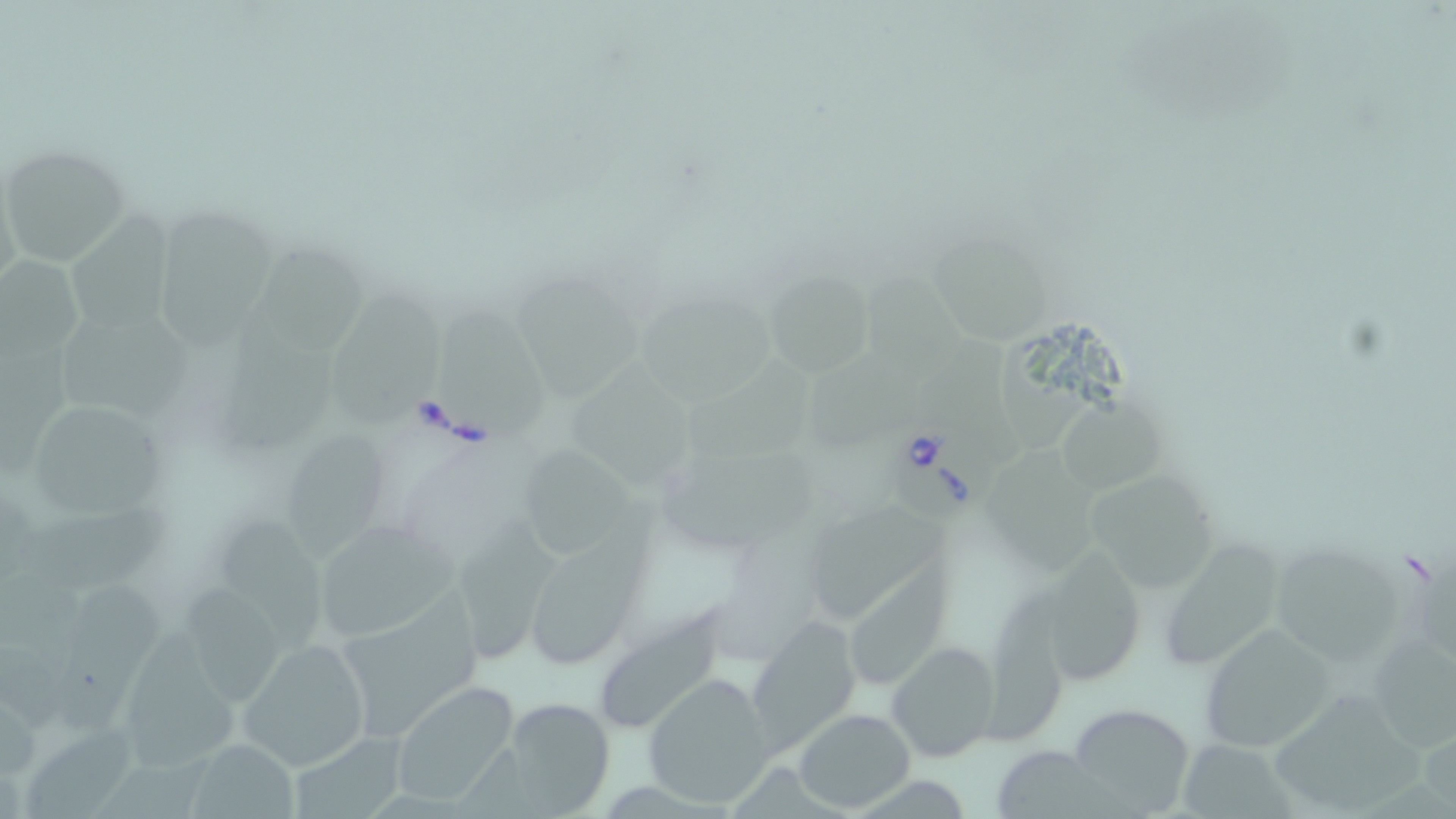

Summary:
  - Coordinate format: approximate bounding boxes as (x1, y1, x2, y2) in pixels
  - Babesia divergens-infected red blood cell locations: (889, 422, 997, 528)
  - Uninfected red blood cell locations: (0, 145, 129, 265), (65, 210, 191, 339), (158, 210, 277, 353), (934, 229, 1051, 347), (262, 245, 365, 353), (1, 254, 84, 360), (513, 271, 644, 409), (764, 272, 876, 375), (332, 276, 444, 427), (866, 279, 967, 378), (640, 288, 776, 409), (438, 299, 553, 435), (59, 308, 202, 425), (219, 311, 344, 454), (918, 334, 1004, 441), (1006, 341, 1095, 446), (0, 344, 76, 481), (692, 353, 820, 474), (569, 358, 696, 487), (813, 362, 923, 447), (1060, 389, 1167, 492), (31, 401, 164, 519), (289, 428, 390, 565), (520, 445, 646, 564), (657, 446, 825, 546), (990, 449, 1108, 570), (1087, 471, 1218, 592), (531, 496, 660, 666), (18, 502, 172, 587), (815, 503, 956, 623), (457, 512, 562, 668), (221, 518, 326, 652), (324, 518, 460, 648), (1163, 529, 1292, 674), (1273, 530, 1407, 674), (1050, 542, 1142, 683), (850, 560, 961, 690), (0, 566, 89, 660), (180, 576, 280, 704), (55, 580, 161, 735), (347, 583, 486, 736), (985, 587, 1077, 745), (603, 600, 730, 729), (749, 618, 861, 749), (1197, 624, 1336, 752), (125, 630, 241, 772), (1373, 635, 1456, 755), (238, 636, 371, 771), (887, 640, 999, 764), (644, 674, 774, 805), (1270, 676, 1418, 810), (391, 680, 521, 807), (515, 702, 620, 818), (1068, 704, 1200, 816), (794, 707, 915, 811), (23, 725, 141, 819), (293, 725, 409, 819), (186, 737, 302, 817), (1182, 742, 1303, 819), (997, 746, 1152, 819), (95, 748, 230, 819), (863, 780, 971, 819)
  - Slide-level diagnosis: Babesia divergens
  - Modality: optical microscopy
  - Stain: May-Grünwald-Giemsa
  - Magnification: 1000x
  - Preparation: thin blood smear
  - Image size: 1456×819 pixels
  - Field of view: single